Comment on the morphology of the red blood cells.
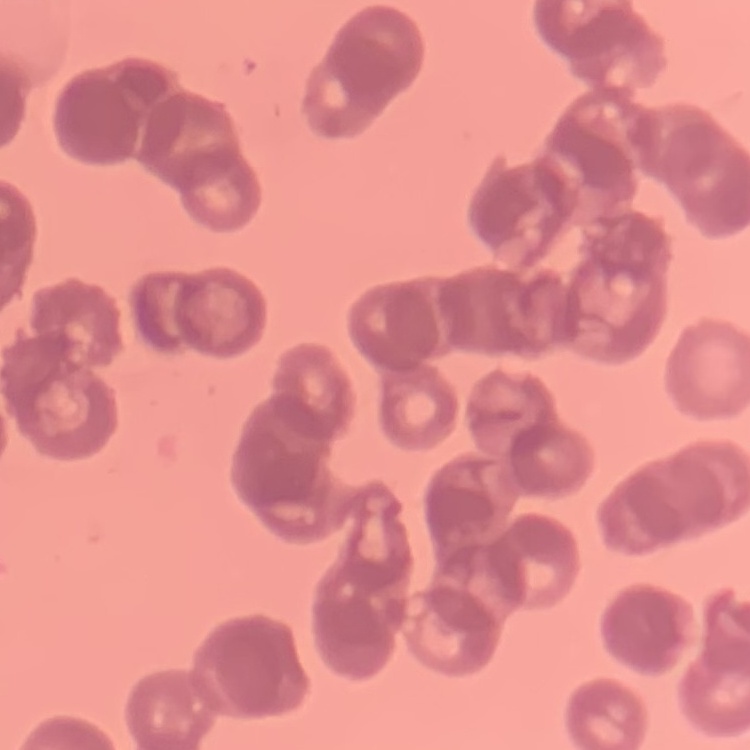
Rouleaux formation.

Summary:
  - Stain: Field's or Giemsa
  - Image type: square crop of a larger photomicrograph
  - Preparation: thin blood film